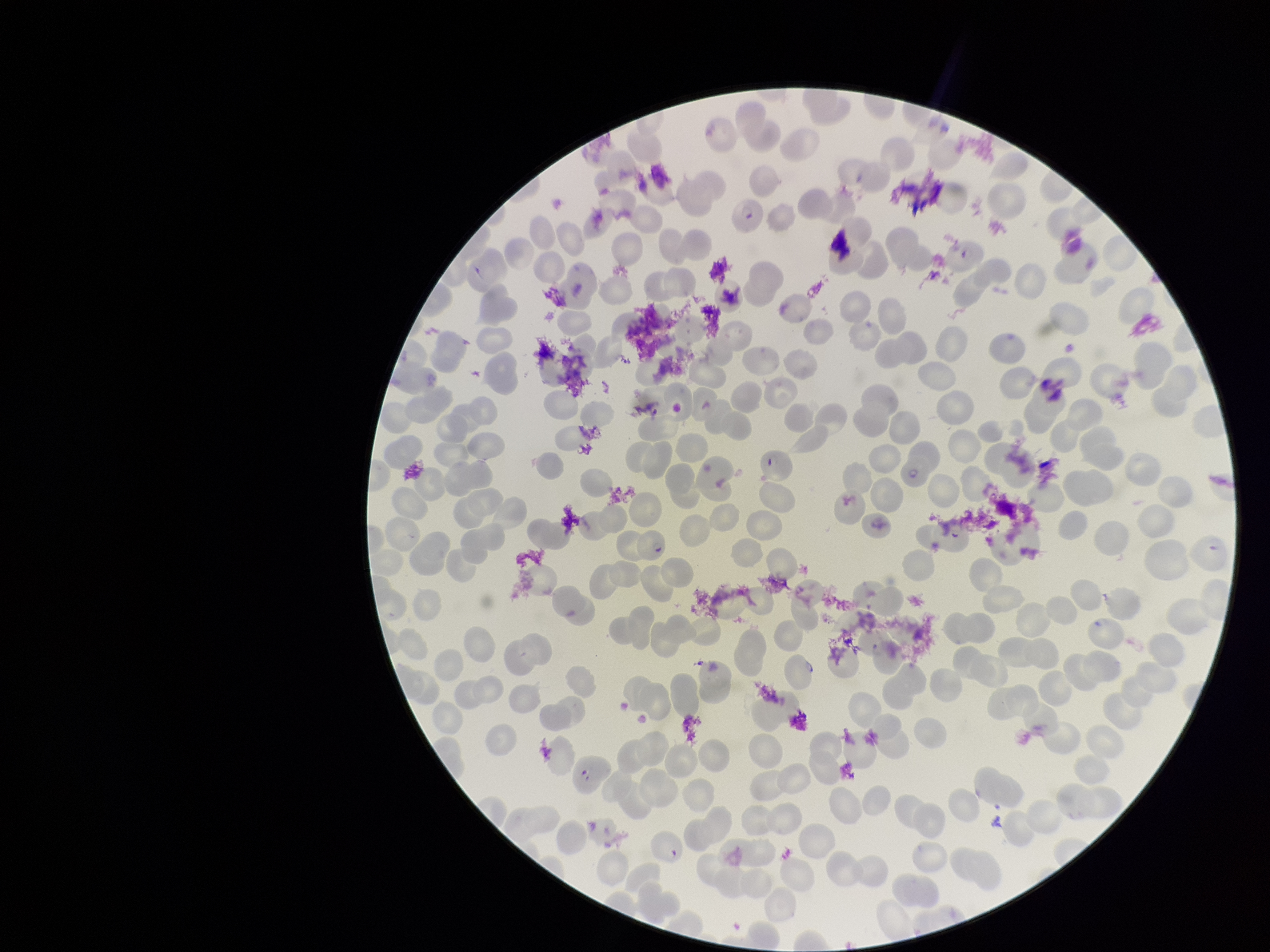
Parasitized red blood cell count: 5. Species reported for this patient: Plasmodium falciparum. Parasitized red blood cells: seen. Image is 1270×952 pixels. One field from this slide. Patient malaria status: positive. Red blood cell count: 274. Smartphone photograph taken through the eyepiece of a microscope. Preparation: thin. Giemsa stain.